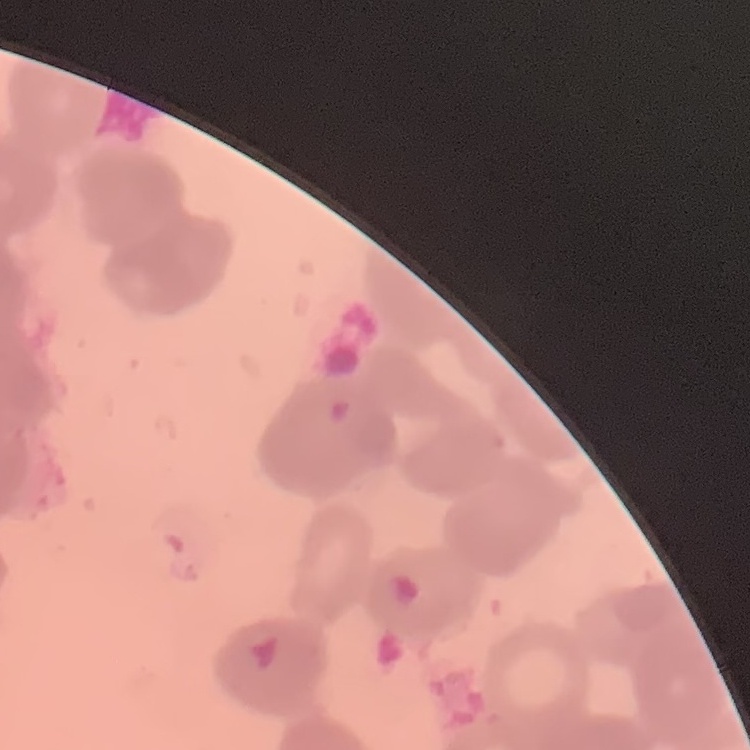
erythrocyte_morphology: rouleaux formation
image_type: one tile cut from a larger photomicrograph
stain: Field's or Giemsa
preparation: thin peripheral smear